Locate every Plasmodium parasite.
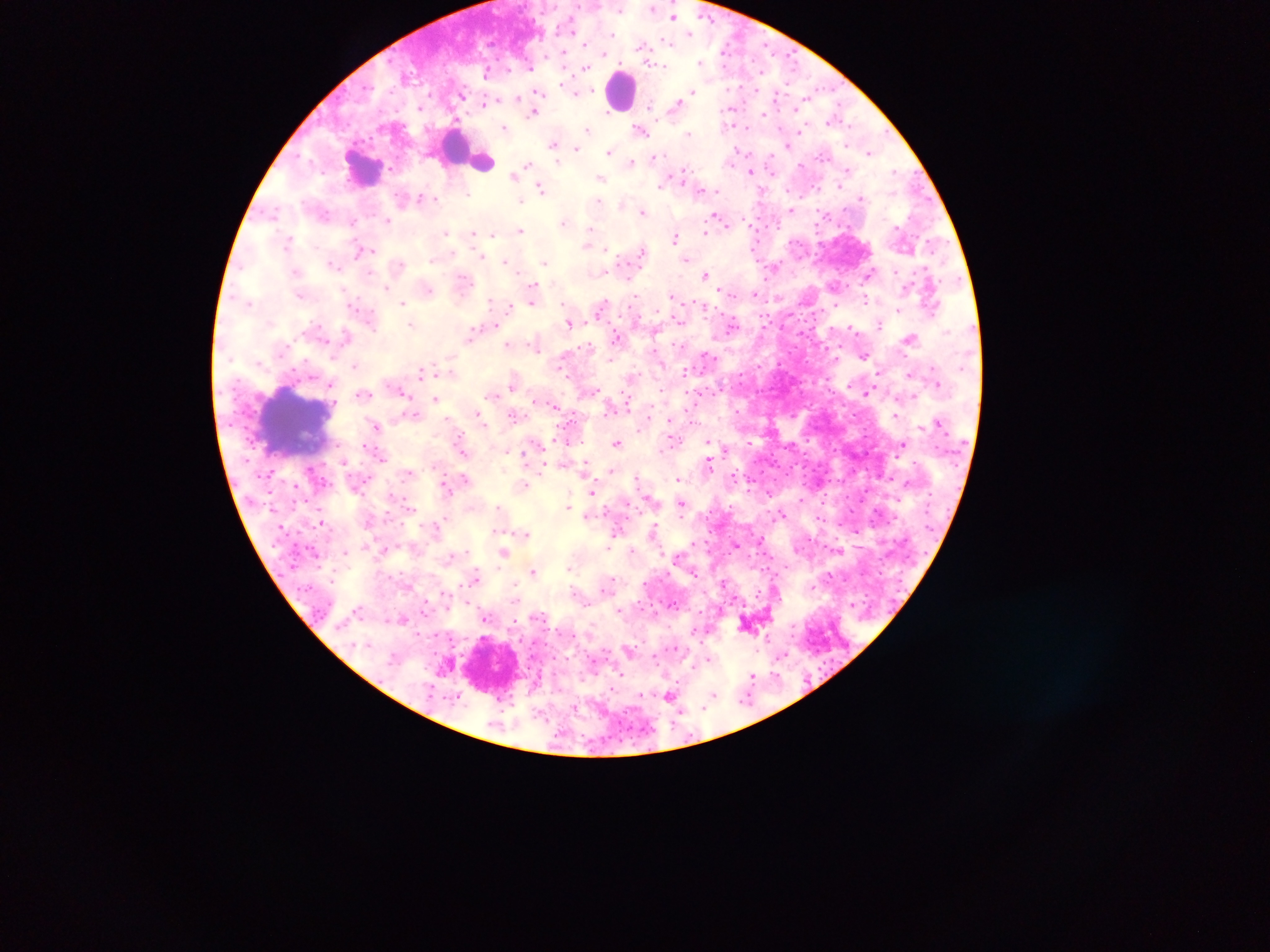

Approximate centers as x y in pixels.
Plasmodium parasites: 619 9; 653 9; 543 12; 673 17; 534 19; 688 32; 571 34; 613 36; 727 43; 585 44; 766 45; 644 46; 720 51; 564 52; 604 54; 773 56; 546 58; 525 59; 754 59; 703 60; 665 65; 724 65; 563 68; 584 68; 532 69; 510 70; 410 72; 762 72; 484 77; 561 82; 741 86; 727 87; 538 90; 693 90; 756 90; 833 90; 592 91; 776 91; 577 92; 429 95; 463 96; 517 99; 804 99; 775 100; 491 101; 673 104; 485 106; 731 107; 418 108; 796 109; 778 111; 608 112; 533 113; 765 114; 657 118; 830 120; 506 126; 587 129; 748 129; 780 129; 642 130; 798 132; 689 133; 553 144; 577 146; 608 152; 734 152; 867 153; 658 156; 768 156; 608 157; 558 161; 529 162; 630 162; 388 170; 751 171; 898 171; 684 172; 513 175; 602 178; 661 186; 541 187; 420 195; 470 195; 435 201; 520 201; 600 202; 621 203; 790 209; 643 210; 717 216; 388 220; 564 221; 722 221; 353 223; 519 230; 447 233; 588 233; 704 233; 473 234; 493 234; 676 238; 287 241; 587 245; 369 249; 643 249; 607 251; 358 252; 453 253; 482 255; 687 259; 432 261; 506 261; 545 262; 332 263; 401 266; 773 268; 370 271; 605 274; 704 274; 868 276; 465 280; 532 282; 835 285; 385 288; 532 288; 430 289; 344 290; 718 291; 756 294; 635 296; 671 296; 778 298; 867 300; 489 302; 533 304; 349 305; 403 305; 511 305; 836 305; 357 310; 371 310; 899 310; 570 322; 586 322; 410 324; 732 324; 878 325; 813 327; 375 329; 831 329; 851 330; 347 333; 471 334; 909 337; 508 344; 796 347; 535 348; 789 354; 863 354; 706 358; 778 365; 354 366; 560 371; 422 372; 513 385; 937 385; 330 387; 401 392; 758 392; 868 392; 406 394; 363 396; 436 397; 556 407; 737 412; 513 415; 896 415; 480 416; 671 422; 377 425; 710 439; 674 440; 616 442; 784 447; 902 447; 524 454; 771 455; 527 459; 710 463; 610 472; 733 472; 787 474; 877 477; 679 479; 591 493; 681 503; 567 505; 497 508; 782 514; 321 522; 653 531; 523 532; 750 533; 762 538; 609 543; 737 544; 607 547; 345 551; 756 551; 504 552; 764 553; 676 554; 747 555; 773 557; 785 568; 568 569; 477 571; 535 572; 475 577; 644 581; 759 589; 775 593; 674 605; 620 609; 486 617; 402 619; 792 625; 693 630; 574 634; 763 635; 793 635; 783 655; 654 660; 824 662; 619 672; 774 672; 581 673; 750 675; 714 693; 670 695; 641 696; 704 709; 681 714; 673 723; 647 730; 619 731; 691 736; 632 740.

Leukocyte locations: 622 87; 453 144; 480 162; 361 170; 293 424. Thick blood smear. Image is 1270×952 pixels. Mobile-phone photograph taken through the microscope. Single field of view. Sample from Ghana.